Outline each blood parasite and name the species.
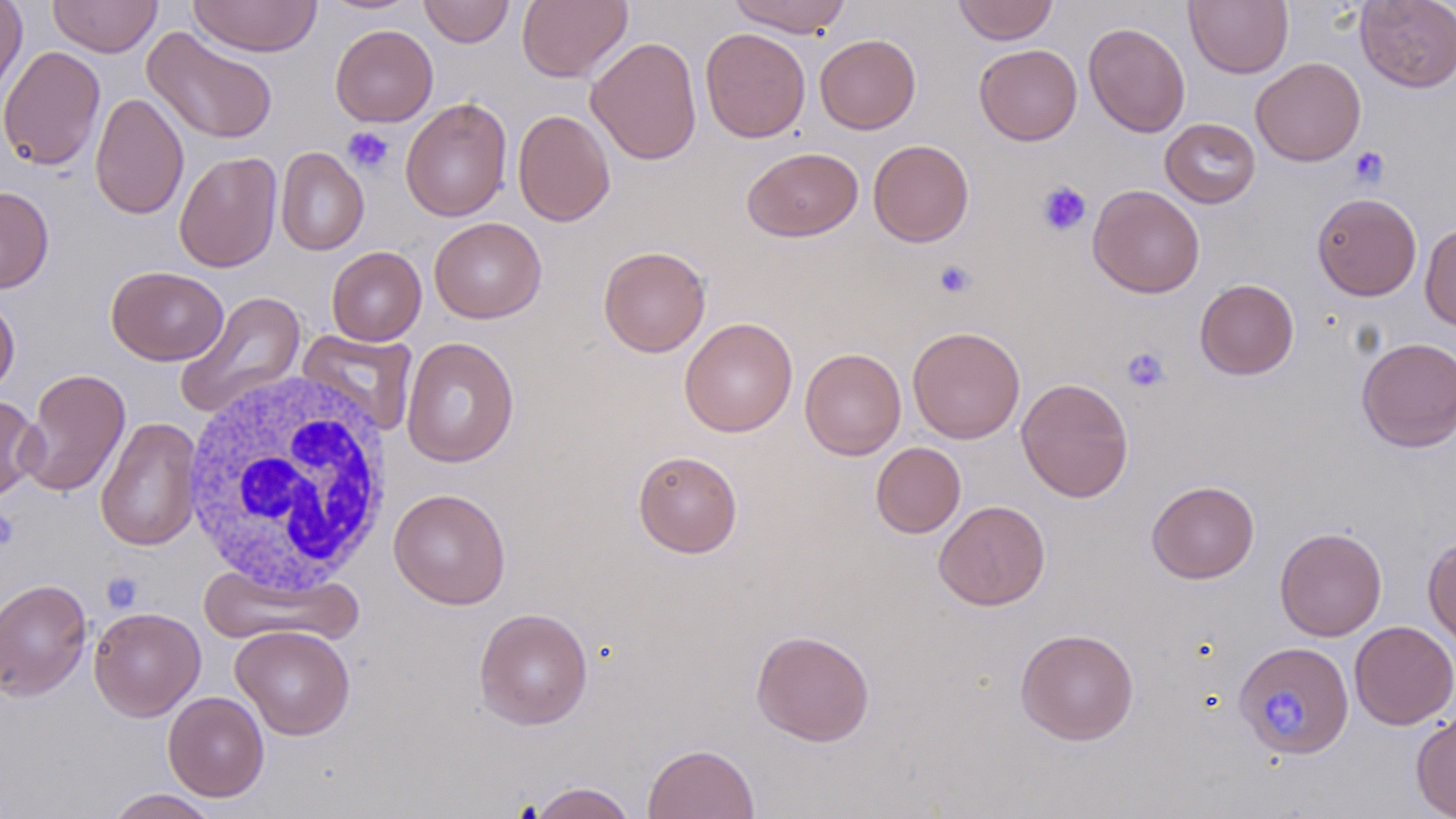
No blood parasites seen.

Approximate bounding boxes as (x1, y1, x2, y2) in pixels. Uninfected red blood cell locations: (0, 0, 28, 103), (48, 0, 162, 57), (188, 0, 322, 57), (317, 0, 423, 14), (419, 0, 515, 47), (518, 0, 632, 83), (727, 0, 852, 36), (952, 0, 1058, 44), (1184, 0, 1294, 78), (1355, 1, 1456, 93), (1083, 22, 1190, 137), (330, 24, 438, 127), (142, 26, 279, 145), (700, 27, 811, 142), (815, 34, 920, 134), (586, 36, 702, 165), (974, 44, 1082, 145), (0, 45, 105, 171), (1250, 57, 1366, 166), (90, 92, 189, 220), (400, 97, 513, 222), (513, 109, 616, 226), (1160, 118, 1260, 208), (867, 139, 974, 247), (742, 146, 863, 242), (276, 147, 369, 255), (174, 151, 282, 272), (1087, 184, 1205, 298), (0, 185, 54, 293), (1311, 192, 1422, 300), (429, 217, 546, 323), (1420, 222, 1456, 331), (597, 245, 711, 357), (327, 246, 426, 346), (106, 266, 228, 365), (1195, 279, 1299, 379), (175, 290, 307, 419), (0, 296, 20, 399), (679, 317, 798, 437), (907, 326, 1025, 443), (297, 329, 419, 436), (401, 336, 520, 468), (1356, 337, 1456, 452), (800, 348, 906, 460), (18, 368, 131, 498), (1016, 377, 1133, 503), (0, 395, 42, 503), (95, 416, 203, 552), (870, 442, 966, 538), (633, 450, 743, 558), (1146, 480, 1259, 583), (388, 488, 511, 609), (934, 500, 1050, 610), (1274, 527, 1387, 641), (1423, 535, 1456, 649), (197, 562, 362, 646), (0, 577, 92, 702), (89, 606, 206, 721), (474, 607, 593, 730), (1349, 621, 1456, 729), (230, 625, 355, 740), (1015, 628, 1139, 745), (751, 629, 875, 746), (1237, 648, 1360, 762), (163, 691, 269, 801), (1411, 708, 1456, 818), (643, 743, 759, 819), (527, 781, 637, 819), (103, 788, 222, 818). White blood cell locations: (179, 369, 398, 596). Platelet locations: (342, 126, 395, 175), (1348, 146, 1389, 187), (1036, 180, 1092, 237), (933, 260, 977, 299), (1122, 347, 1172, 393), (0, 508, 19, 551), (101, 570, 144, 613), (1264, 689, 1314, 741). Slide-level diagnosis: negative for blood parasites. May-Grünwald-Giemsa-stained preparation. Image is 1456×819 pixels. Single field of view. Thin blood smear. Captured at 1000x magnification. Light microscopy.